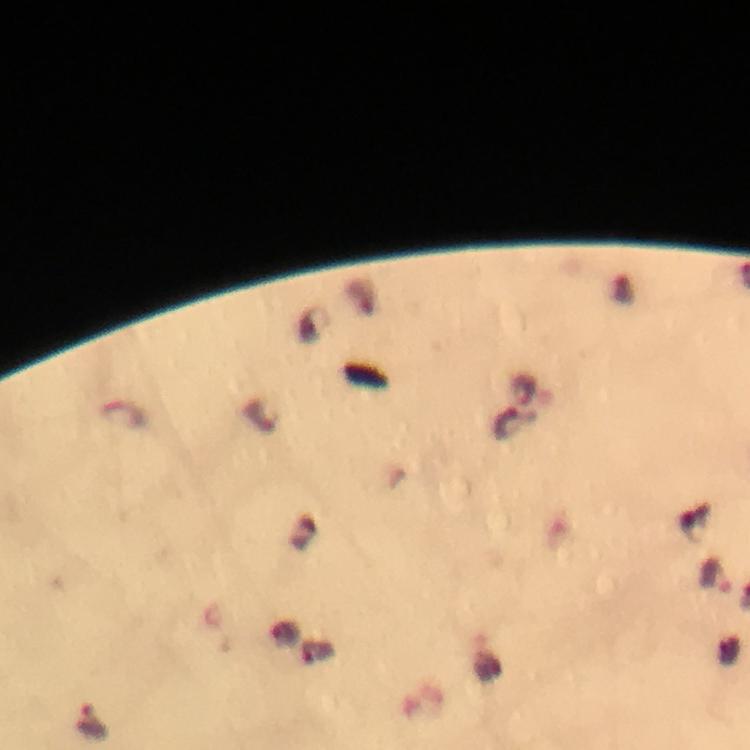

{
  "stain": "Giemsa",
  "preparation": "thick blood film",
  "immersion_oil": "used",
  "cropped_from": "a single field of view",
  "plasmodium_parasite_locations": "approximate object centers, in pixels from the top-left corner: (x=507, y=425), (x=715, y=577), (x=88, y=721)",
  "magnification": "100x",
  "capture": "smartphone photograph through a microscope",
  "image_size": "750×750 pixels",
  "context": "from a diagnostic examination for malaria"
}